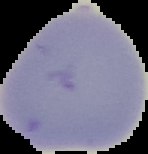
image type = cell region segmented out of the field of view; surrounding area masked to black
result = no Plasmodium parasites detected
image size = 148×154 pixels
preparation = thin blood film